Locate platelets.
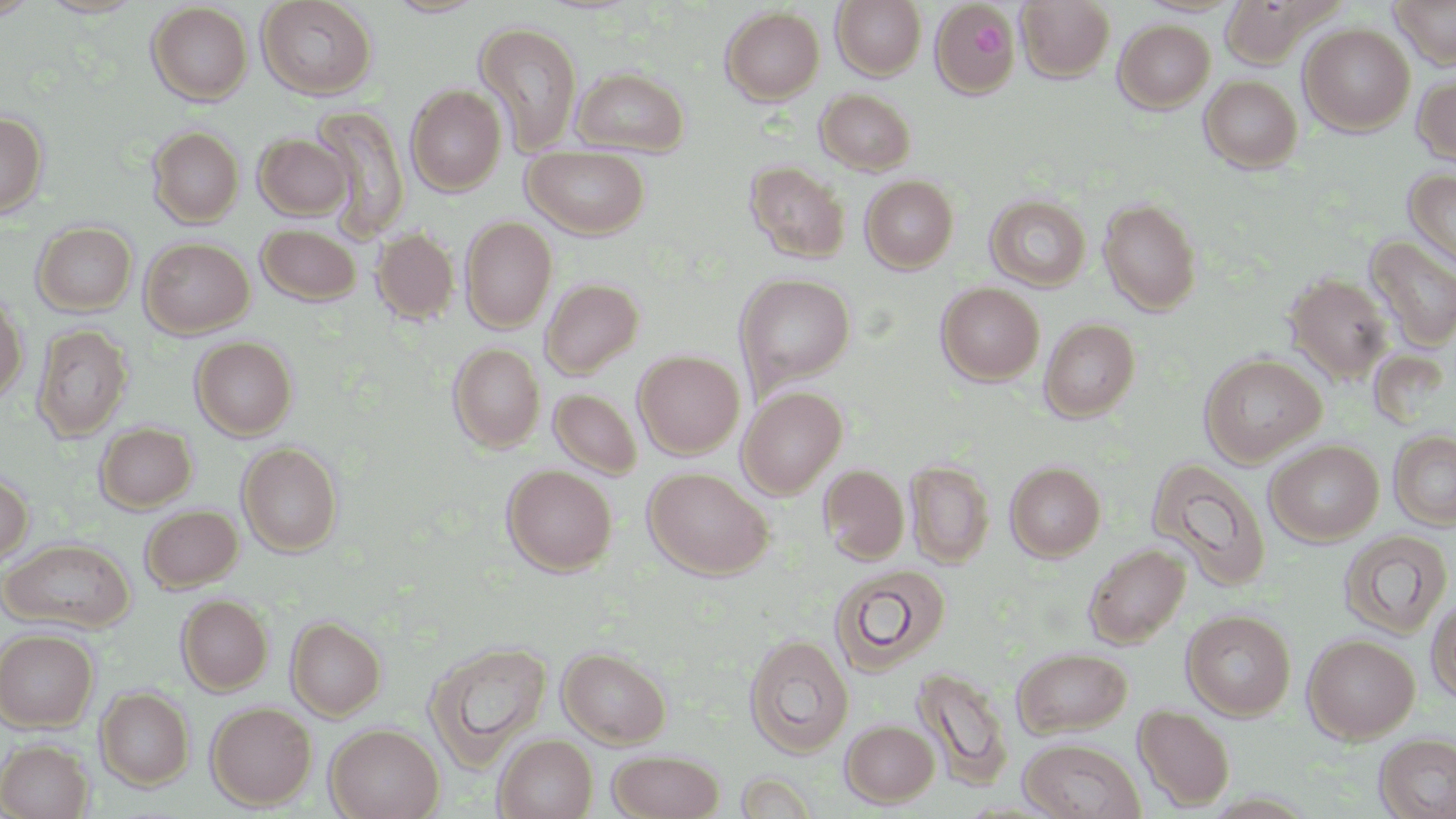
Approximate bounding boxes as [x1, y1, x2, y2] in pixels.
Platelets: [972, 23, 1005, 58].

Summary:
  - Uninfected red blood cell locations: [0, 0, 40, 21], [37, 0, 146, 19], [256, 0, 378, 100], [383, 0, 488, 18], [1017, 0, 1115, 82], [1389, 0, 1456, 69], [832, 1, 926, 80], [1221, 1, 1315, 67], [929, 2, 1021, 98], [146, 3, 252, 106], [720, 6, 824, 105], [1114, 20, 1215, 113], [474, 21, 583, 155], [1299, 24, 1415, 135], [572, 66, 690, 155], [1413, 72, 1456, 167], [1199, 74, 1303, 173], [406, 85, 507, 195], [816, 88, 916, 175], [310, 106, 410, 241], [0, 112, 47, 220], [148, 126, 244, 227], [254, 132, 353, 219], [524, 147, 650, 238], [746, 162, 849, 263], [1403, 168, 1456, 273], [861, 175, 959, 273], [986, 195, 1091, 292], [1098, 198, 1202, 316], [460, 216, 557, 333], [32, 222, 137, 316], [257, 224, 361, 305], [371, 227, 460, 324], [1364, 235, 1456, 351], [141, 237, 254, 337], [1285, 272, 1394, 384], [735, 273, 856, 392], [541, 278, 644, 378], [936, 283, 1044, 385], [0, 292, 28, 406], [1039, 317, 1141, 422], [32, 323, 133, 442], [191, 336, 298, 439], [448, 343, 545, 453], [633, 350, 744, 458], [1199, 353, 1327, 466], [737, 385, 848, 499], [549, 389, 642, 479], [95, 423, 197, 512], [1389, 429, 1456, 530], [1265, 439, 1384, 546], [237, 442, 343, 556], [1147, 457, 1272, 590], [905, 460, 994, 567], [1005, 462, 1105, 561], [502, 465, 617, 575], [819, 465, 909, 565], [643, 467, 774, 579], [0, 468, 33, 568], [140, 504, 242, 591], [1337, 529, 1453, 639], [1, 538, 135, 633], [1084, 543, 1190, 648], [829, 563, 951, 676], [176, 594, 273, 695], [1426, 594, 1456, 703], [1181, 609, 1295, 720], [286, 616, 386, 721], [0, 628, 99, 731], [744, 634, 854, 757], [1303, 634, 1419, 743], [425, 640, 552, 768], [557, 646, 671, 747], [1012, 647, 1132, 738], [912, 665, 1015, 791], [96, 687, 194, 789], [206, 702, 316, 809], [1134, 704, 1235, 811], [840, 719, 939, 807], [325, 723, 444, 819], [1374, 732, 1456, 819], [494, 734, 597, 818], [0, 738, 93, 818], [1018, 739, 1146, 819], [608, 749, 725, 818], [734, 771, 818, 818]
  - Slide-level diagnosis: negative for blood parasites
  - Image size: 1456×819 pixels
  - Preparation: thin blood film
  - Magnification: 1000x
  - Field of view: one of a larger specimen
  - Stain: May-Grünwald-Giemsa
  - Modality: optical microscopy